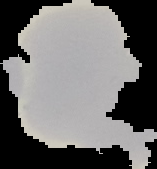 Malaria status: uninfected. Image is 157×169 pixels. Cell region segmented out of the field of view; the surrounding area is masked to black. From a thin blood film.